Classify this cell by malaria status.
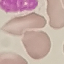

Uninfected.

Photographed with a smartphone camera at the microscope eyepiece. Cell patch, automatically extracted from a larger field of view and resized to 64 × 64 pixels. Thin blood film. Giemsa-stained preparation.